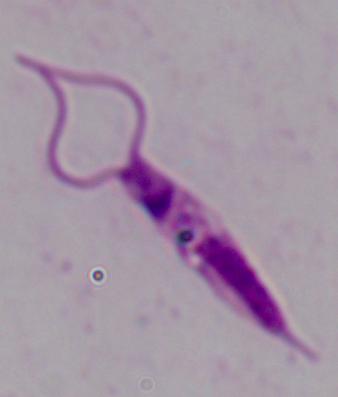
Summary:
  - Magnification: 1000x
  - Identification: Leishmania
  - Modality: photomicrograph